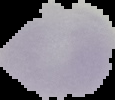

From a thin blood film. Result: negative for malaria parasites. Image is 115×100 pixels. The area outside the segmented cell region is set to black.